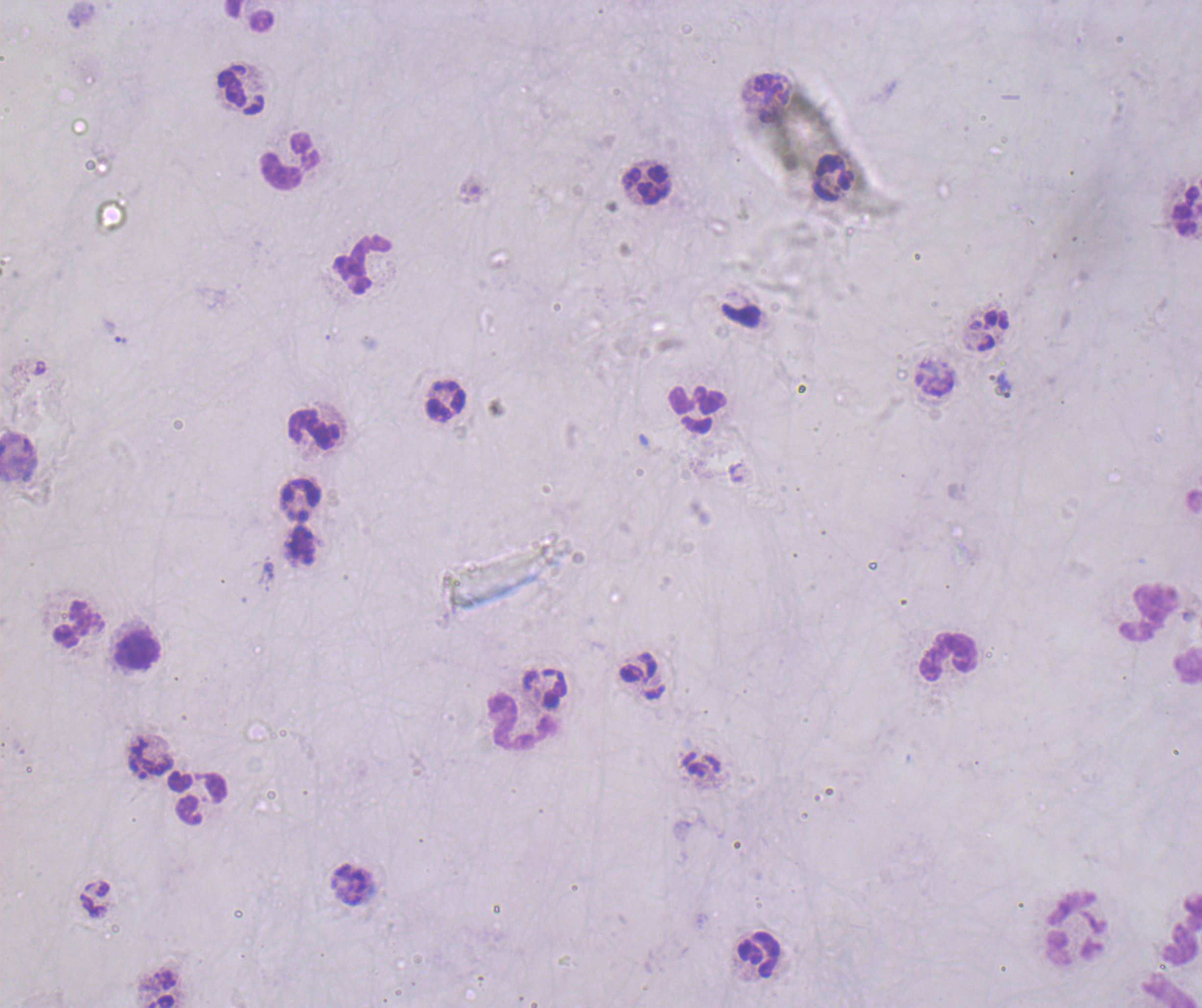
Approximate object centers, in pixels from the top-left corner. Leukocyte locations: (x=241, y=91), (x=290, y=162), (x=833, y=176), (x=646, y=185), (x=1186, y=209), (x=362, y=264), (x=445, y=400), (x=696, y=410), (x=314, y=429), (x=299, y=500), (x=1150, y=611), (x=79, y=624), (x=137, y=650), (x=947, y=656), (x=523, y=722), (x=202, y=799), (x=1076, y=926), (x=1181, y=929), (x=758, y=954). Captured at 100x magnification. Previously used in a real diagnosis. Result: negative for malaria parasites. Image is 1202×1008 pixels. Coloration quality: bad. Romanowsky stain. Background quality: poor. Thick blood film. Single field of view.